Report the malaria status of this cell.
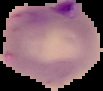
Parasitized.

{
  "image_size": "103×91 pixels",
  "preparation": "thin blood film",
  "image_type": "segmented cell region with the area outside set to black"
}